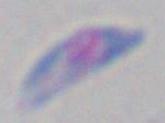
Summary:
  - Modality: photomicrograph
  - Identification: Toxoplasma gondii
  - Magnification: 1000x